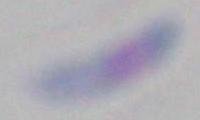
Summary:
  - Modality: photomicrograph
  - Magnification: 1000x
  - Identification: Toxoplasma gondii